Identify the parasite.
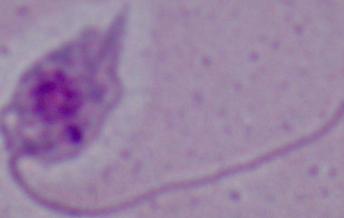

Leishmania.

Photomicrograph. 1000x magnification.